Assess the morphology of the erythrocytes.
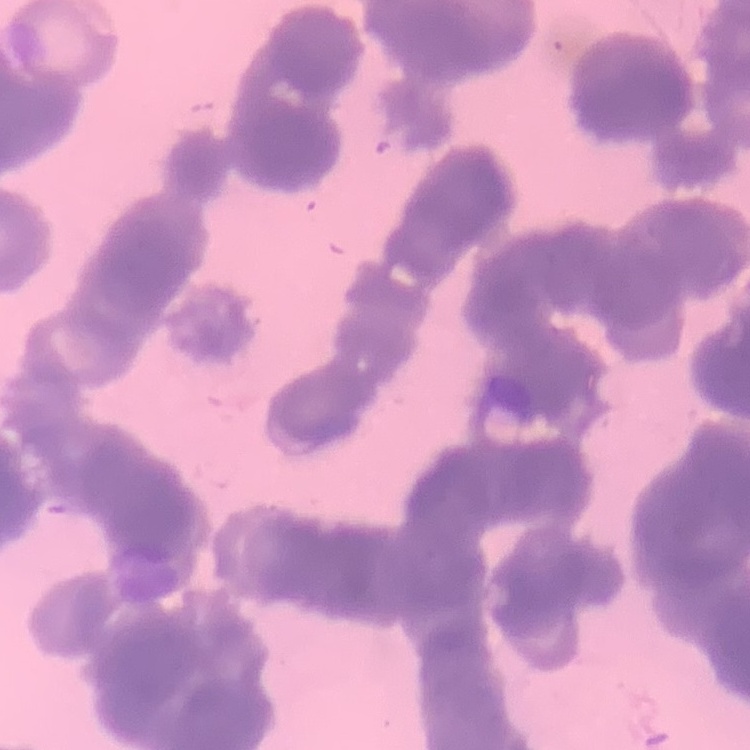
They show rouleaux formation.

Field's or Giemsa stain. Thin blood smear. One tile cut from a larger photomicrograph.